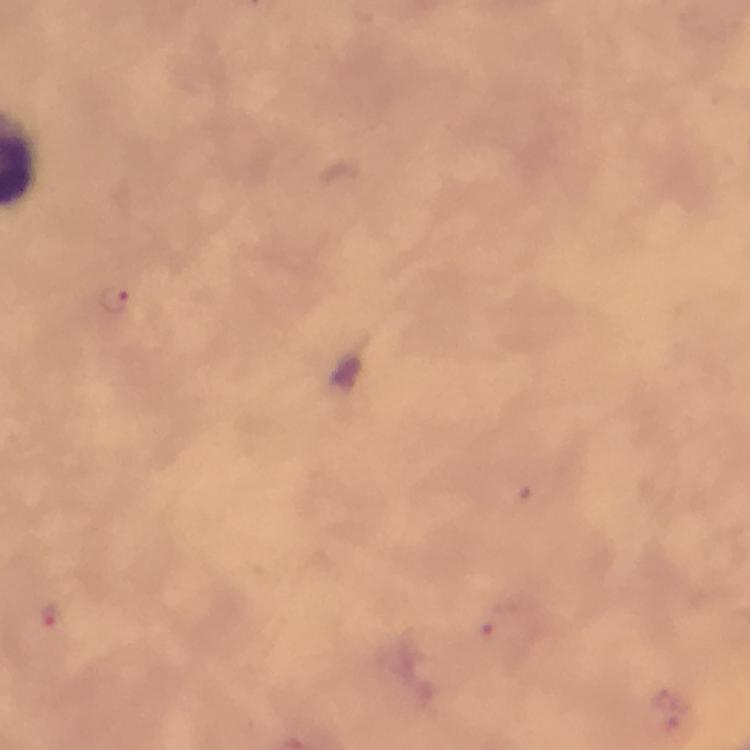

Approximate centers as (x, y) in pixels.
Summary:
  - Malaria parasite locations: (115, 300), (48, 613), (496, 620)
  - Immersion oil: used
  - Capture: smartphone camera through the microscope
  - Context: from a diagnostic examination for malaria
  - Stain: Giemsa
  - Cropped from: a single field of view
  - Magnification: 100x
  - Image size: 750×750 pixels
  - Preparation: thick blood smear